Assess the morphology of the red blood cells.
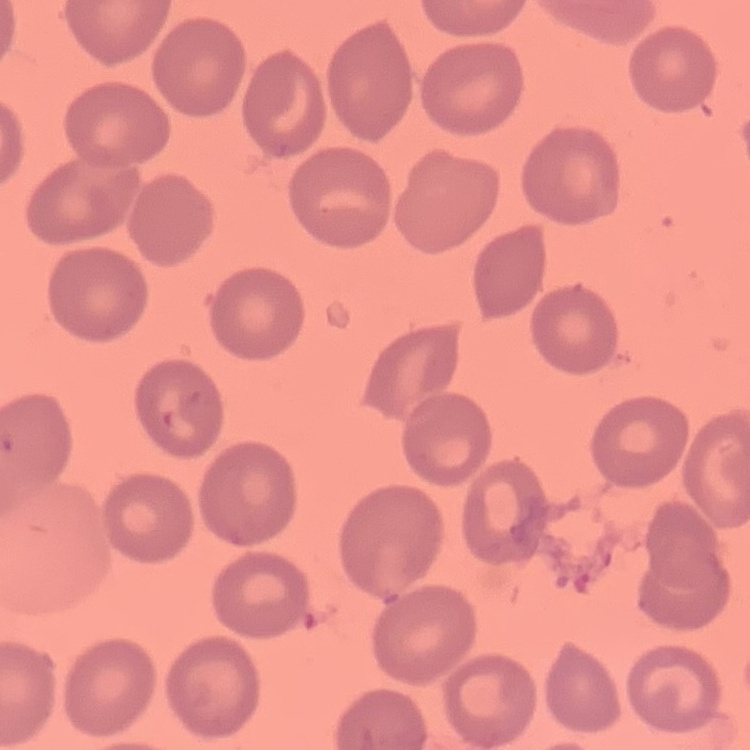
They show no rouleaux formation.

Summary:
  - Image type: square crop of a larger photomicrograph
  - Preparation: thin blood smear
  - Stain: Field's or Giemsa